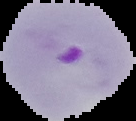 Image is 136×121 pixels. From a thin blood film. Malaria status: parasitized. Cell region segmented out of the field of view; the surrounding area is masked to black.